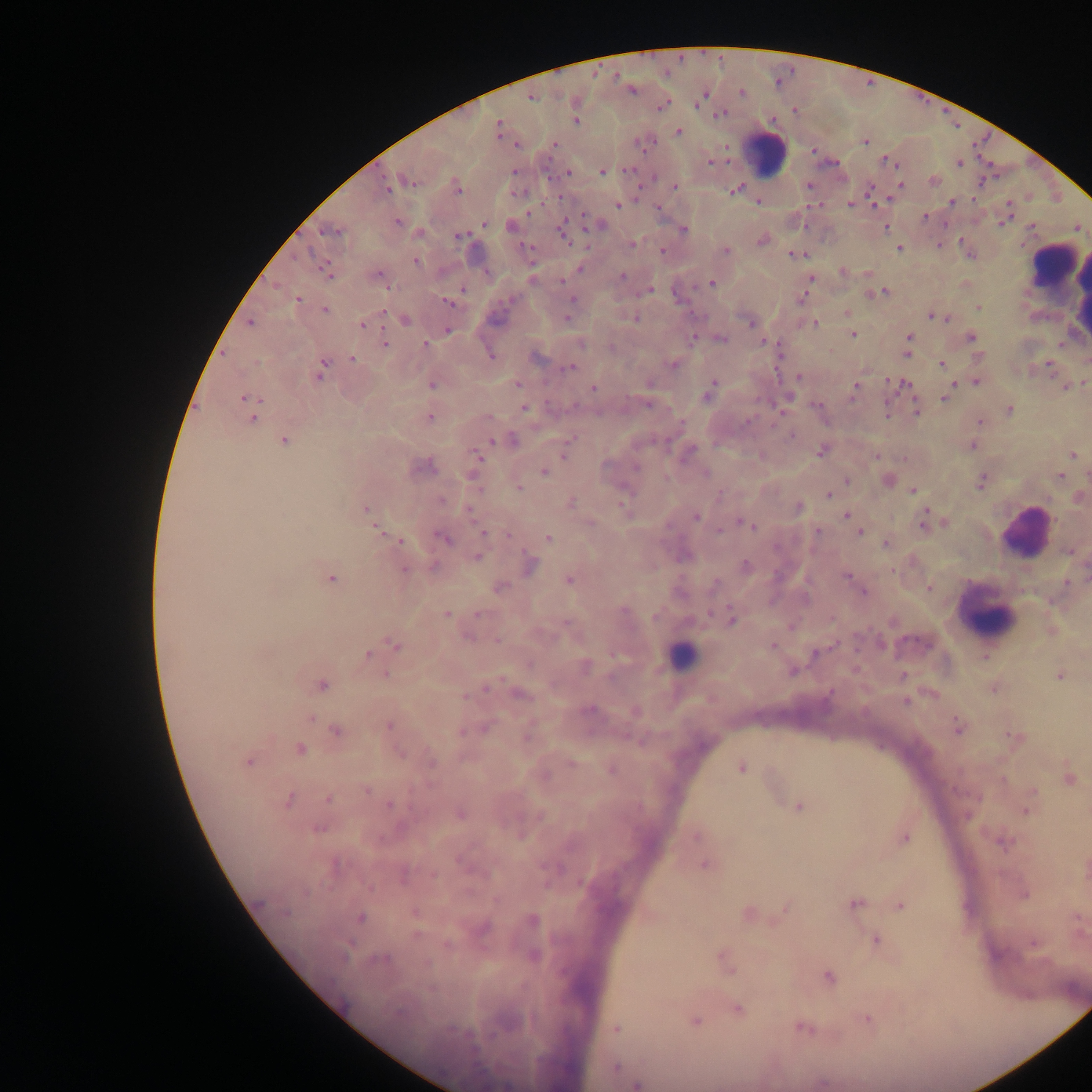
Approximate centers as [x, y] in pixels.
Summary:
  - Plasmodium parasite locations: [631, 89], [703, 95], [530, 97], [661, 105], [721, 114], [574, 120], [499, 129], [678, 132], [865, 141], [516, 144], [554, 144], [814, 150], [710, 161], [959, 162], [893, 163], [630, 170], [568, 171], [603, 171], [406, 181], [934, 181], [808, 185], [900, 185], [387, 187], [674, 187], [457, 188], [733, 191], [758, 200], [951, 202], [851, 203], [618, 205], [657, 207], [924, 217], [1005, 218], [398, 222], [484, 224], [597, 224], [886, 227], [1076, 227], [512, 228], [331, 230], [683, 230], [564, 234], [459, 236], [761, 240], [631, 244], [898, 248], [662, 251], [725, 251], [798, 255], [416, 262], [325, 268], [580, 269], [842, 271], [378, 275], [622, 276], [811, 278], [711, 283], [809, 283], [965, 284], [649, 289], [882, 292], [874, 293], [805, 294], [297, 299], [447, 301], [978, 307], [325, 310], [847, 313], [567, 316], [934, 316], [635, 318], [941, 318], [404, 319], [750, 321], [250, 322], [813, 323], [362, 324], [447, 330], [852, 334], [693, 335], [971, 337], [720, 338], [908, 338], [764, 342], [384, 343], [770, 343], [425, 345], [906, 353], [491, 355], [534, 356], [979, 357], [352, 359], [673, 364], [941, 364], [1048, 364], [569, 367], [321, 371], [798, 377], [976, 381], [1084, 382], [431, 383], [952, 383], [517, 384], [903, 385], [855, 386], [1066, 386], [593, 387], [709, 391], [945, 397], [247, 399], [785, 400], [647, 403], [818, 406], [524, 408], [1009, 410], [916, 411], [253, 415], [429, 417], [979, 422], [792, 434], [283, 440], [509, 440], [567, 444], [971, 445], [821, 450], [688, 451], [1072, 454], [876, 456], [477, 458], [422, 466], [543, 471], [1059, 475], [846, 480], [887, 480], [981, 481], [518, 487], [913, 489], [829, 494], [1078, 497], [569, 502], [622, 506], [798, 507], [364, 509], [469, 510], [846, 514], [696, 517], [923, 522], [742, 523], [750, 525], [377, 529], [817, 530], [860, 531], [483, 534], [508, 534], [443, 537], [547, 538], [399, 540], [886, 544], [1070, 551], [477, 557], [530, 565], [745, 566], [404, 569], [848, 576], [331, 577], [569, 579], [498, 587], [929, 588], [863, 591], [446, 614], [478, 614], [731, 619], [568, 625], [881, 644], [395, 645], [772, 646], [816, 653], [367, 655], [985, 657], [584, 666], [792, 670], [386, 674], [902, 675], [1059, 675], [321, 685], [486, 687], [993, 687], [518, 694], [906, 701], [588, 709], [635, 710], [388, 725], [957, 726], [484, 728], [336, 730], [527, 734], [1014, 737], [299, 749], [248, 761], [431, 762], [741, 767], [611, 769], [1068, 778], [365, 790], [329, 798], [287, 799], [389, 806], [798, 806], [1026, 810], [459, 814], [318, 827], [697, 835], [904, 837], [1003, 842], [704, 863], [1024, 894], [854, 903], [899, 905], [785, 906], [415, 912], [747, 914], [359, 917], [532, 921], [481, 927], [876, 940], [1033, 942], [532, 956], [724, 961], [828, 977], [737, 1009], [868, 1019], [694, 1020], [802, 1027], [615, 1029], [615, 1067], [637, 1084]
  - Leukocyte locations: [764, 154], [1052, 263], [1080, 286], [1027, 533], [986, 614], [682, 656], [1073, 990]
  - Image size: 1092×1092 pixels
  - Country: Ghana
  - Capture: mobile-phone photograph through a microscope
  - Preparation: thick blood smear
  - Field of view: single